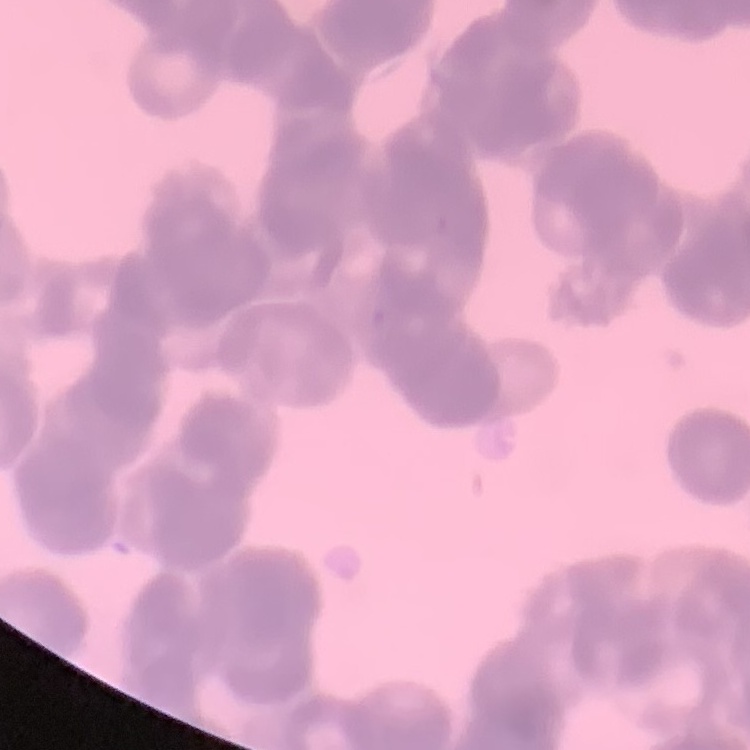
red blood cell morphology = rouleaux formation
preparation = thin peripheral smear
stain = Field's or Giemsa
image type = square crop of a larger photomicrograph